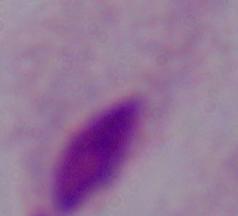
A trichomonad is shown. Captured at 1000x magnification. Photomicrograph.